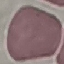

Malaria status: uninfected. Giemsa-stained preparation. Acquired by smartphone through the microscope eyepiece. Cell patch, automatically extracted from a larger field of view and resized to 64 × 64 pixels. Thin blood smear.